Classify this cell by malaria status.
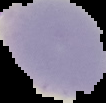

It is parasitized.

Summary:
  - Image type: cell region segmented out of the field of view; surrounding area masked to black
  - Preparation: thin blood film
  - Image size: 106×103 pixels